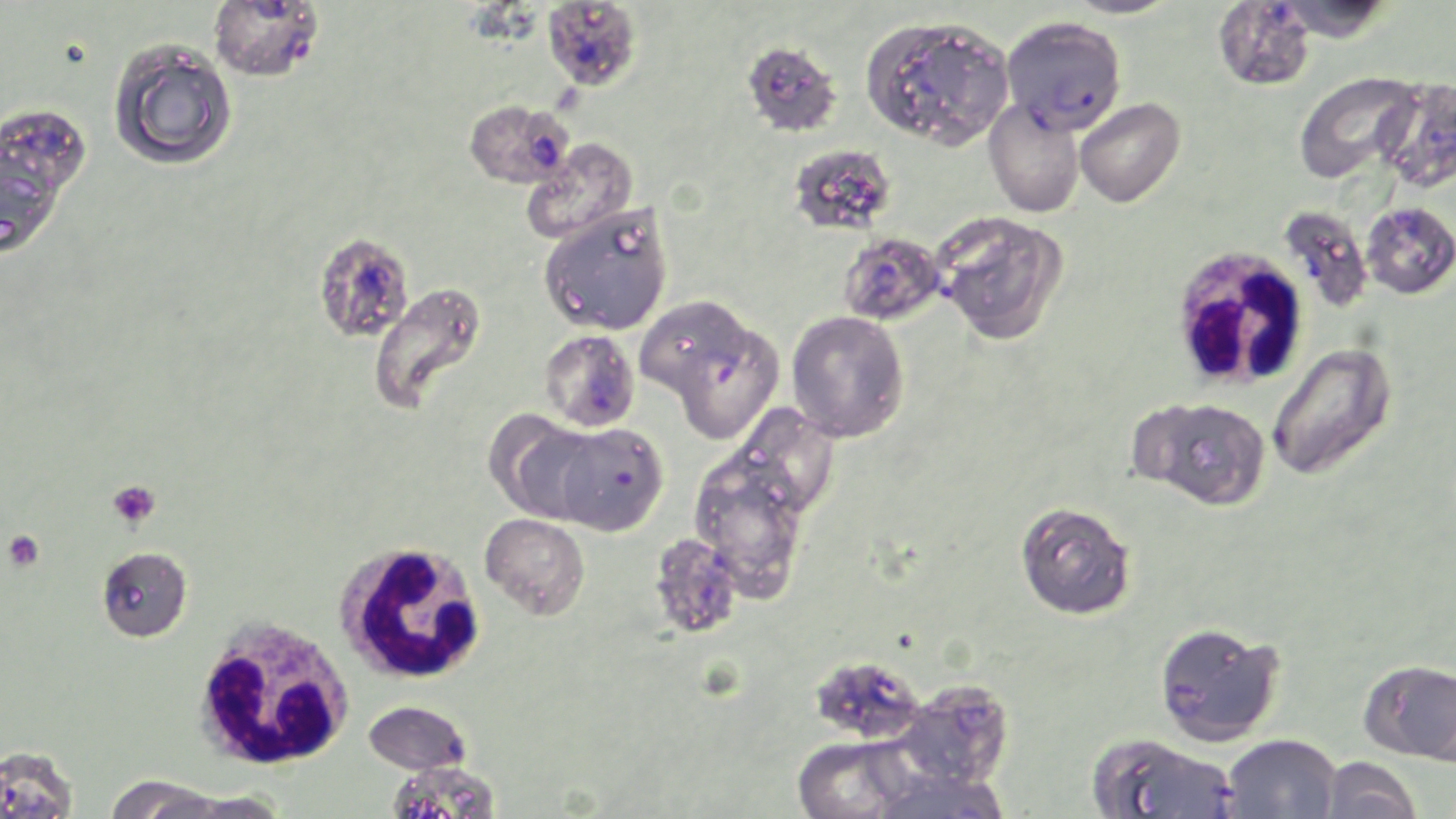

Summary:
  - Coordinate format: approximate bounding boxes as named x1/y1/x2/y2 corners in pixels
  - Uninfected red blood cell locations: (x1=1061, y1=0, x2=1183, y2=19), (x1=1272, y1=0, x2=1395, y2=43), (x1=1212, y1=1, x2=1316, y2=92), (x1=860, y1=14, x2=1014, y2=150), (x1=108, y1=40, x2=239, y2=171), (x1=740, y1=40, x2=842, y2=137), (x1=1295, y1=71, x2=1422, y2=186), (x1=1376, y1=79, x2=1456, y2=193), (x1=1075, y1=98, x2=1186, y2=208), (x1=984, y1=99, x2=1084, y2=218), (x1=1, y1=104, x2=93, y2=202), (x1=520, y1=138, x2=638, y2=245), (x1=788, y1=143, x2=897, y2=236), (x1=0, y1=146, x2=66, y2=259), (x1=539, y1=202, x2=674, y2=337), (x1=1361, y1=202, x2=1456, y2=299), (x1=935, y1=211, x2=1069, y2=346), (x1=367, y1=281, x2=487, y2=415), (x1=786, y1=311, x2=910, y2=443), (x1=1267, y1=343, x2=1397, y2=481), (x1=1134, y1=396, x2=1271, y2=511), (x1=485, y1=412, x2=603, y2=524), (x1=688, y1=449, x2=812, y2=600), (x1=1015, y1=501, x2=1136, y2=620), (x1=480, y1=513, x2=591, y2=620), (x1=648, y1=533, x2=743, y2=640), (x1=96, y1=546, x2=192, y2=642), (x1=1153, y1=621, x2=1285, y2=747), (x1=1360, y1=658, x2=1456, y2=764), (x1=811, y1=666, x2=924, y2=738), (x1=892, y1=680, x2=1016, y2=790), (x1=362, y1=700, x2=472, y2=776), (x1=1087, y1=731, x2=1239, y2=818), (x1=1221, y1=733, x2=1340, y2=819), (x1=791, y1=736, x2=917, y2=819), (x1=1320, y1=756, x2=1423, y2=818), (x1=386, y1=760, x2=502, y2=819), (x1=866, y1=768, x2=1012, y2=819), (x1=102, y1=775, x2=230, y2=818), (x1=166, y1=791, x2=290, y2=818)
  - Platelet locations: (x1=108, y1=481, x2=160, y2=529), (x1=3, y1=530, x2=44, y2=572)
  - White blood cell locations: (x1=1178, y1=250, x2=1306, y2=383), (x1=336, y1=539, x2=487, y2=686), (x1=192, y1=614, x2=356, y2=772)
  - Plasmodium falciparum-infected red blood cell locations: (x1=208, y1=1, x2=325, y2=83), (x1=541, y1=1, x2=643, y2=92), (x1=1001, y1=15, x2=1127, y2=134), (x1=462, y1=99, x2=576, y2=189), (x1=1281, y1=206, x2=1371, y2=312), (x1=312, y1=232, x2=415, y2=344), (x1=837, y1=232, x2=945, y2=326), (x1=642, y1=301, x2=753, y2=404), (x1=538, y1=330, x2=640, y2=433), (x1=550, y1=422, x2=668, y2=537), (x1=0, y1=745, x2=78, y2=819)
  - Slide-level diagnosis: Plasmodium falciparum
  - Field of view: single
  - Preparation: thin blood smear
  - Stain: May-Grünwald-Giemsa
  - Image size: 1456×819 pixels
  - Magnification: 1000x
  - Modality: light microscopy